Comment on the morphology of the erythrocytes.
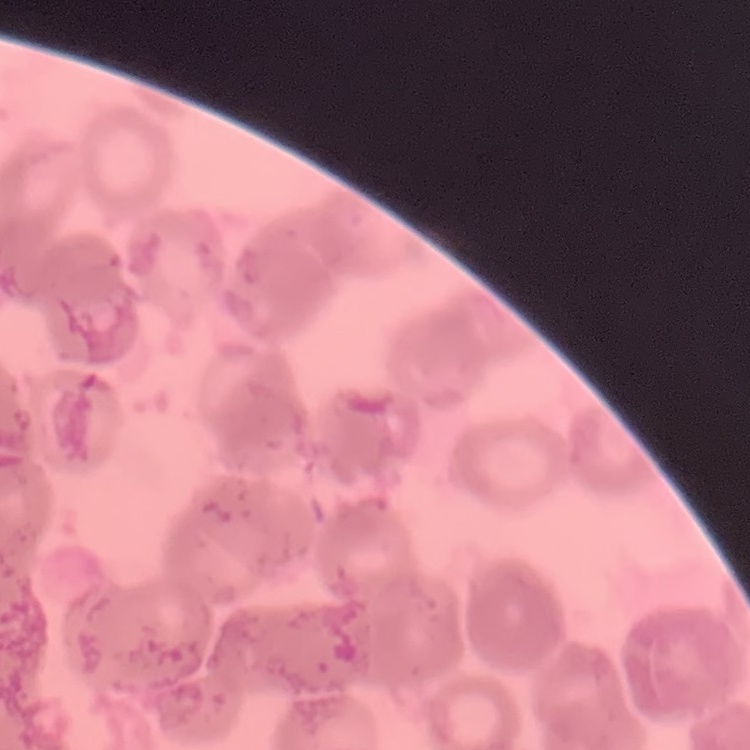
Rouleaux formation.

Summary:
  - Stain: Field's or Giemsa
  - Preparation: thin peripheral smear
  - Image type: one tile cut from a larger photomicrograph